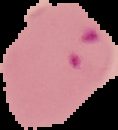
preparation = thin blood film
image type = segmented cell region with the area outside set to black
image size = 118×130 pixels
malaria status = parasitized